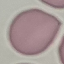

result: no malaria parasites seen
capture: smartphone through the microscope eyepiece
image_type: automatically extracted cell patch, resized to 64 × 64 pixels
stain: Giemsa
preparation: thin blood film